Classify this cell by malaria status.
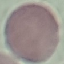
It is uninfected.

preparation = thin blood smear
capture = smartphone camera at the microscope eyepiece
image type = cell patch, automatically extracted from a larger field of view and resized to 64 × 64 pixels
stain = Giemsa